Report the malaria status of this cell.
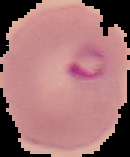

Parasitized.

Summary:
  - Preparation: thin blood film
  - Image size: 130×157 pixels
  - Image type: cell region segmented out of the field of view; surrounding area masked to black